Identify the parasite.
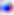

This is Toxoplasma gondii.

400x magnification. Photomicrograph.